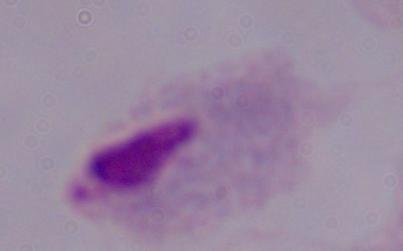

Summary:
  - Magnification: 1000x
  - Modality: photomicrograph
  - Identification: trichomonad